Classify this cell by malaria status.
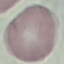

Uninfected.

Summary:
  - Preparation: thin blood smear
  - Stain: Giemsa
  - Image type: cell patch, automatically extracted from a larger field of view and resized to 64 × 64 pixels
  - Capture: smartphone through the microscope eyepiece